Name the blood parasite species.
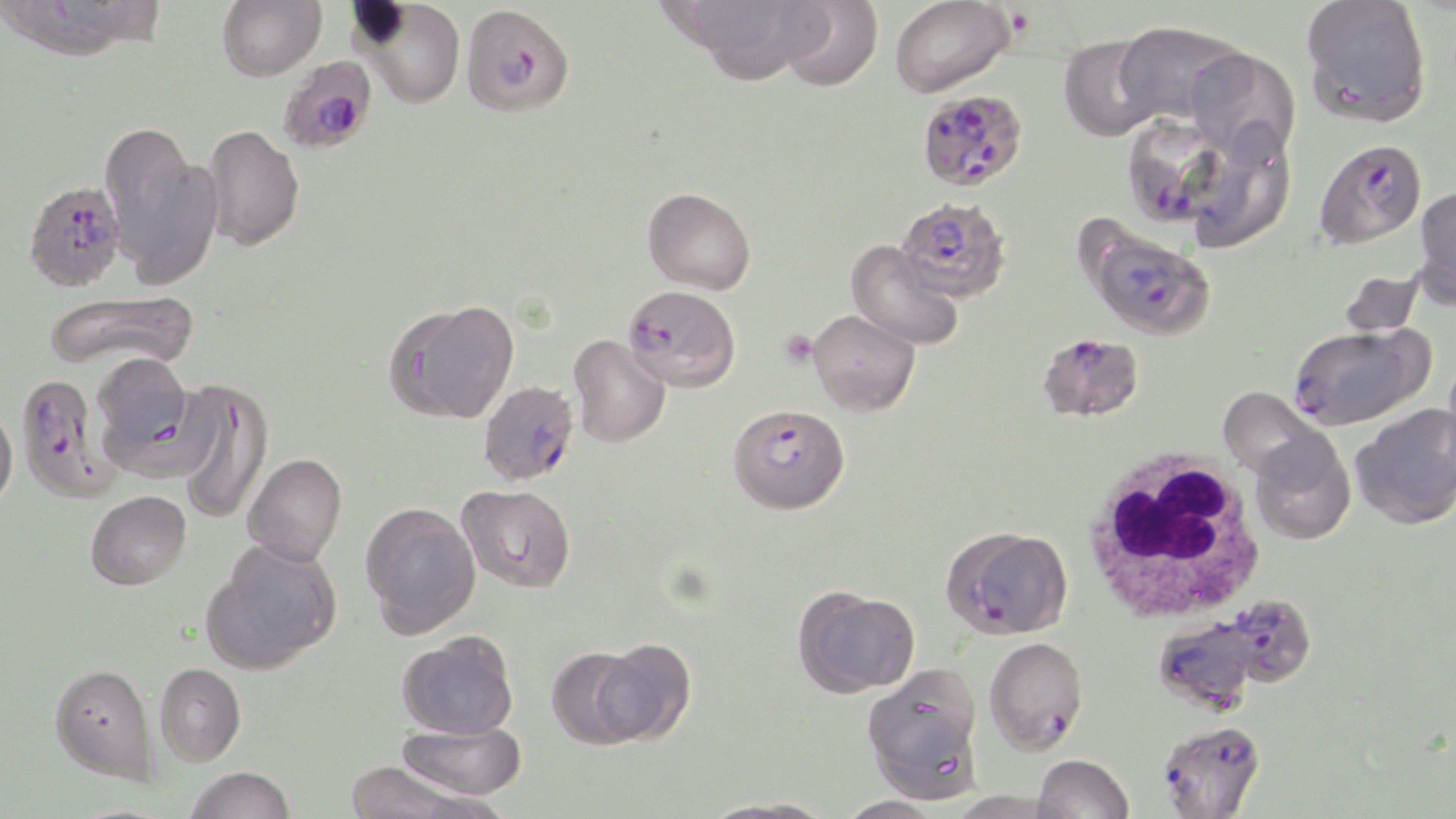
Plasmodium falciparum.

preparation = thin blood smear
modality = light microscopy
uninfected red blood cell locations = approximate bounding boxes as (x1, y1, x2, y2) in pixels: (217, 0, 326, 81), (356, 0, 466, 108), (687, 0, 793, 63), (777, 0, 883, 91), (890, 0, 1015, 98), (1299, 0, 1432, 128), (1114, 20, 1246, 126), (1059, 35, 1162, 141), (1185, 47, 1301, 161), (203, 123, 305, 250), (104, 128, 221, 290), (1413, 185, 1456, 305), (643, 187, 756, 294), (846, 239, 964, 351), (1338, 269, 1425, 339), (41, 289, 200, 373), (386, 300, 519, 424), (808, 309, 920, 416), (567, 334, 671, 447), (90, 354, 206, 479), (175, 379, 274, 526), (1218, 386, 1326, 482), (0, 403, 18, 512), (1349, 404, 1456, 529), (1249, 431, 1355, 545), (243, 453, 347, 565), (457, 483, 576, 593), (85, 490, 191, 590), (360, 501, 480, 637), (205, 538, 343, 673), (794, 586, 919, 697), (398, 630, 519, 739), (592, 637, 696, 744), (546, 646, 646, 747), (50, 662, 158, 782), (154, 662, 246, 766), (861, 663, 984, 803), (397, 722, 526, 800), (1033, 753, 1134, 819), (344, 760, 496, 819), (185, 766, 295, 819), (836, 796, 944, 818), (697, 797, 838, 818)
platelet locations = approximate bounding boxes as (x1, y1, x2, y2) in pixels: (780, 330, 818, 367)
white blood cell locations = approximate bounding boxes as (x1, y1, x2, y2) in pixels: (1080, 447, 1268, 625)
stain = May-Grünwald-Giemsa
magnification = 1000x
image size = 1456×819 pixels
Plasmodium falciparum-infected red blood cell locations = approximate bounding boxes as (x1, y1, x2, y2) in pixels: (461, 3, 575, 116), (277, 55, 377, 155), (917, 89, 1028, 191), (1123, 109, 1226, 229), (1313, 139, 1426, 247), (26, 188, 128, 299), (896, 196, 1011, 302), (1091, 231, 1216, 340), (623, 284, 741, 392), (1288, 326, 1422, 429), (1037, 332, 1145, 422), (15, 371, 123, 502), (478, 380, 579, 486), (729, 404, 850, 514), (941, 525, 1073, 639), (1224, 593, 1316, 687), (1152, 616, 1259, 713), (983, 636, 1088, 755), (1157, 719, 1266, 819)
field of view = single